Assess this cell for malaria.
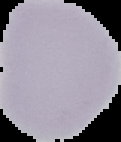
Uninfected.

Summary:
  - Preparation: thin blood film
  - Image type: segmented cell region with the area outside set to black
  - Image size: 121×142 pixels